Outline each uninfected red blood cell.
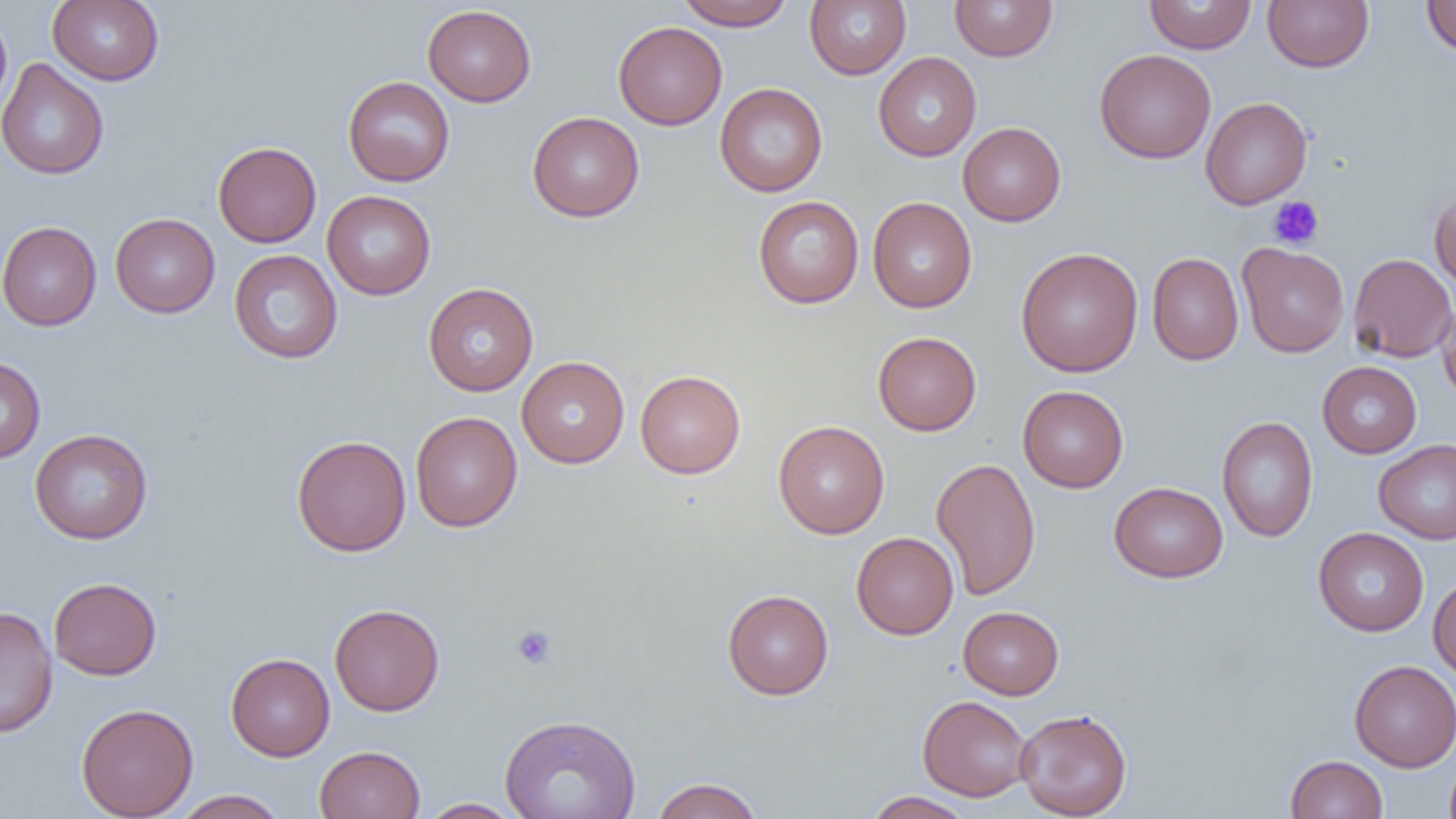
Approximate bounding boxes as (x1, y1, x2, y2) in pixels.
Uninfected red blood cells: (48, 0, 164, 85), (675, 0, 793, 30), (1144, 0, 1256, 54), (1262, 0, 1373, 73), (1422, 0, 1456, 57), (805, 1, 911, 79), (949, 1, 1057, 61), (422, 4, 536, 106), (0, 7, 13, 123), (613, 21, 727, 130), (1094, 49, 1216, 163), (873, 52, 981, 161), (0, 59, 109, 180), (343, 76, 455, 186), (715, 83, 828, 197), (1200, 96, 1313, 209), (527, 111, 645, 222), (958, 122, 1066, 226), (213, 141, 321, 247), (322, 190, 436, 299), (1429, 190, 1456, 294), (752, 196, 864, 308), (868, 197, 976, 313), (110, 213, 220, 318), (0, 221, 101, 331), (1237, 243, 1349, 357), (1015, 247, 1143, 377), (229, 249, 342, 364), (1147, 252, 1244, 365), (1348, 253, 1456, 362), (423, 282, 538, 396), (1436, 300, 1456, 404), (873, 331, 982, 436), (0, 356, 45, 464), (517, 356, 629, 468), (1317, 361, 1421, 458), (635, 370, 746, 478), (1018, 385, 1128, 492), (410, 412, 522, 532), (1216, 416, 1319, 542), (773, 420, 890, 538), (29, 428, 153, 544), (292, 434, 411, 557), (1373, 438, 1456, 544), (931, 457, 1041, 601), (1109, 481, 1228, 583), (1314, 527, 1429, 636), (851, 532, 958, 639), (1428, 575, 1456, 682), (49, 577, 161, 680), (722, 589, 834, 699), (330, 603, 445, 716), (1, 605, 58, 739), (958, 606, 1064, 699), (226, 653, 335, 760), (1349, 660, 1456, 771), (918, 695, 1033, 801), (76, 703, 198, 818), (1015, 708, 1132, 818), (499, 713, 641, 819), (314, 745, 426, 819), (1444, 754, 1456, 819), (1285, 755, 1388, 818), (650, 778, 764, 819), (171, 790, 289, 818), (862, 791, 975, 819), (418, 798, 524, 818).

slide-level diagnosis = negative for blood parasites
modality = optical microscopy
platelet locations = approximate bounding boxes as (x1, y1, x2, y2) in pixels: (1268, 196, 1324, 249), (512, 625, 557, 669)
field of view = one of a larger specimen
image size = 1456×819 pixels
magnification = 1000x
preparation = thin blood film